Name the cell type shown.
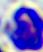

This is a leukocyte.

modality = photomicrograph
magnification = 400x